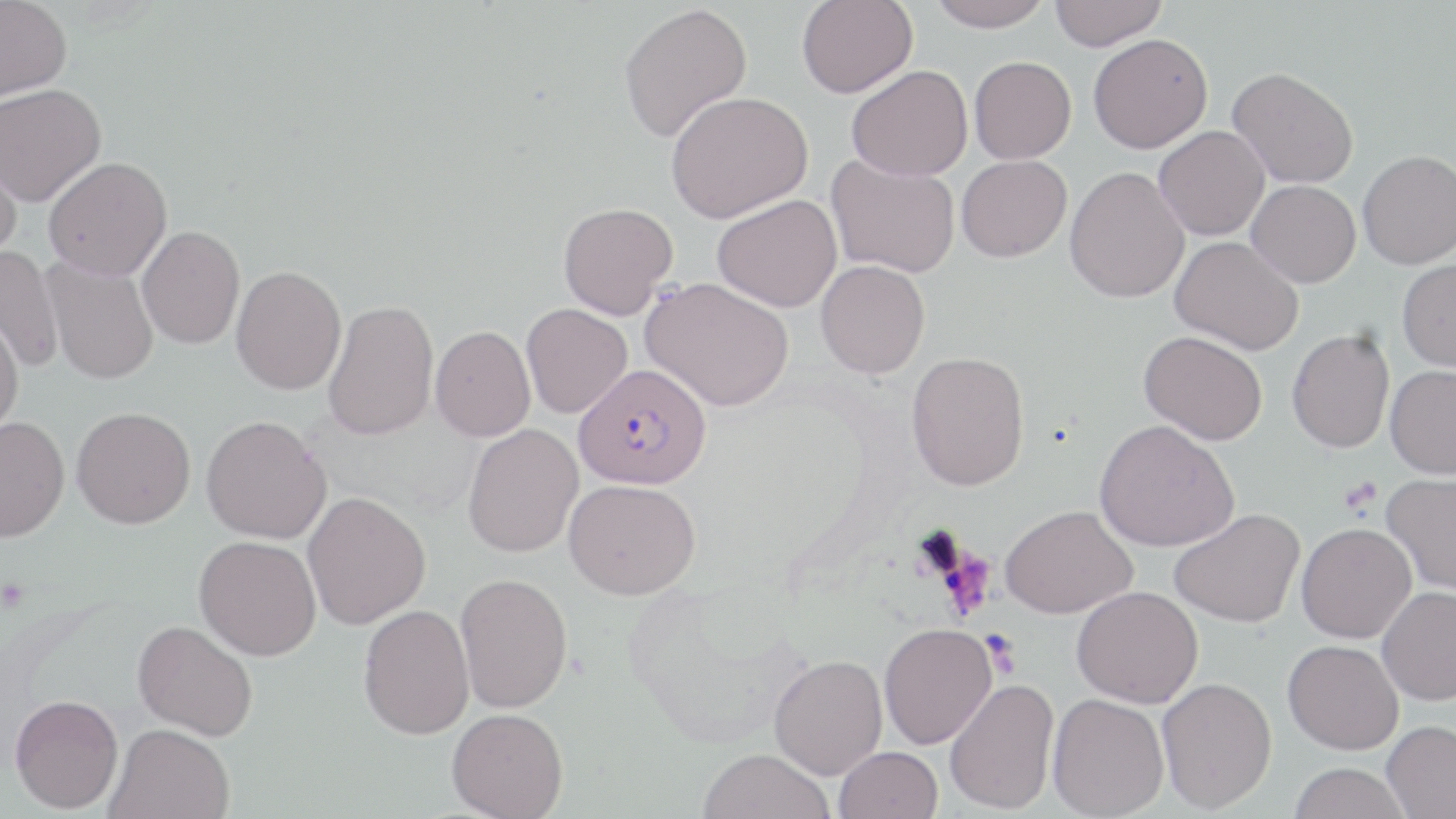

Summary:
  - Coordinate format: approximate bounding boxes as (x1, y1, x2, y2) in pixels
  - Uninfected red blood cell locations: (0, 0, 72, 101), (797, 0, 917, 98), (927, 0, 1053, 31), (1048, 0, 1166, 50), (618, 3, 753, 143), (1088, 33, 1213, 153), (969, 56, 1077, 164), (846, 65, 973, 181), (1227, 67, 1359, 188), (0, 83, 106, 207), (666, 91, 813, 223), (1154, 126, 1269, 241), (0, 143, 24, 261), (1357, 150, 1456, 269), (956, 155, 1071, 262), (43, 156, 172, 281), (827, 156, 960, 278), (1065, 166, 1190, 303), (1247, 180, 1361, 288), (712, 194, 842, 313), (558, 202, 678, 319), (137, 225, 245, 349), (1170, 235, 1303, 355), (0, 246, 64, 374), (41, 256, 159, 385), (1397, 258, 1456, 372), (816, 260, 930, 378), (230, 266, 347, 395), (641, 276, 794, 411), (322, 299, 439, 441), (521, 303, 633, 418), (0, 310, 24, 437), (431, 325, 536, 442), (1286, 329, 1395, 453), (1139, 331, 1267, 445), (906, 351, 1030, 491), (1385, 364, 1456, 479), (71, 406, 196, 528), (201, 415, 332, 544), (0, 417, 70, 542), (1094, 420, 1239, 552), (462, 424, 584, 558), (1381, 471, 1456, 594), (564, 478, 701, 599), (302, 491, 431, 630), (1001, 505, 1137, 618), (1170, 508, 1305, 627), (1296, 523, 1417, 643), (194, 535, 322, 661), (454, 571, 573, 714), (1072, 585, 1203, 708), (1377, 586, 1456, 705), (358, 604, 474, 739), (133, 619, 258, 741), (879, 622, 997, 749), (1283, 639, 1403, 754), (769, 654, 888, 779), (1157, 677, 1277, 812), (944, 678, 1059, 814), (1047, 693, 1169, 818), (9, 694, 124, 813), (447, 707, 568, 819), (1382, 719, 1456, 818), (105, 722, 235, 818), (833, 745, 942, 819), (698, 748, 836, 819), (1288, 762, 1411, 819)
  - Plasmodium falciparum-infected red blood cell locations: (573, 363, 712, 489)
  - Platelet locations: (1339, 476, 1383, 515)
  - Slide-level diagnosis: Plasmodium falciparum
  - Modality: optical microscopy
  - Field of view: single
  - Magnification: 1000x
  - Stain: May-Grünwald-Giemsa
  - Image size: 1456×819 pixels
  - Preparation: thin blood film